Classify this cell by malaria status.
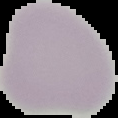

Uninfected.

Image is 118×118 pixels. The area outside the segmented cell region is set to black. From a thin blood film.